Identify the parasite.
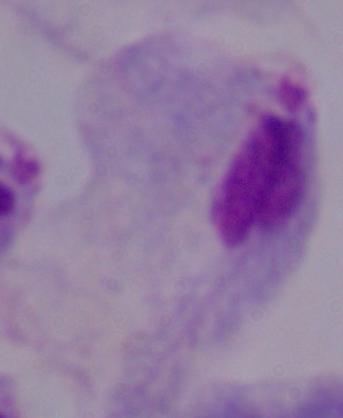

This is a trichomonad.

Captured at 1000x magnification. Photomicrograph.